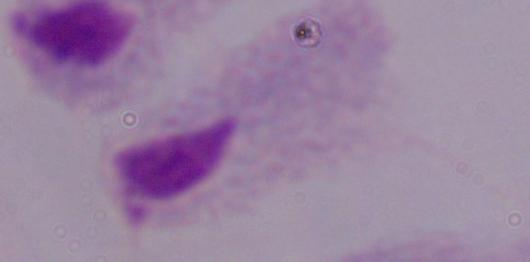
Summary:
  - Magnification: 1000x
  - Identification: trichomonad
  - Modality: photomicrograph